Mark where leukocytes are.
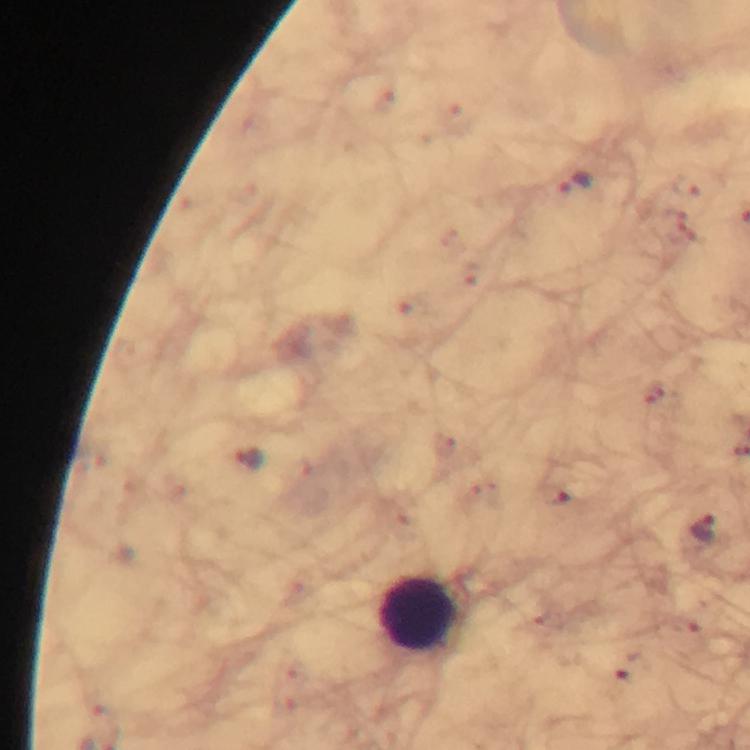

Approximate centers as (x, y) in pixels.
Leukocytes: (419, 613).

Malaria parasite locations: (575, 185), (247, 458), (704, 530). Immersion oil applied. Smartphone photograph taken through a microscope. Giemsa-stained preparation. A crop from one field of view. At 100x magnification. Image is 750×750 pixels. From a malaria diagnostic workup. Thick blood smear.